Assess this cell for malaria.
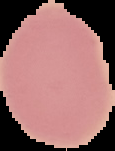
Uninfected.

Summary:
  - Image size: 115×151 pixels
  - Image type: cell region segmented out of the field of view; surrounding area masked to black
  - Preparation: thin blood smear